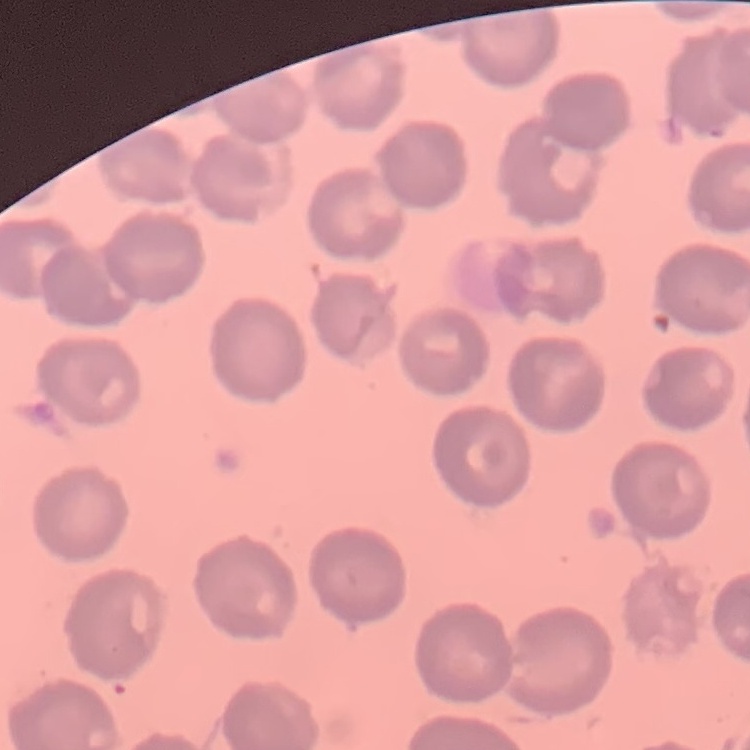
Summary:
  - Erythrocyte morphology: no rouleaux formation
  - Preparation: thin blood film
  - Image type: one tile cut from a larger photomicrograph
  - Stain: Field's or Giemsa